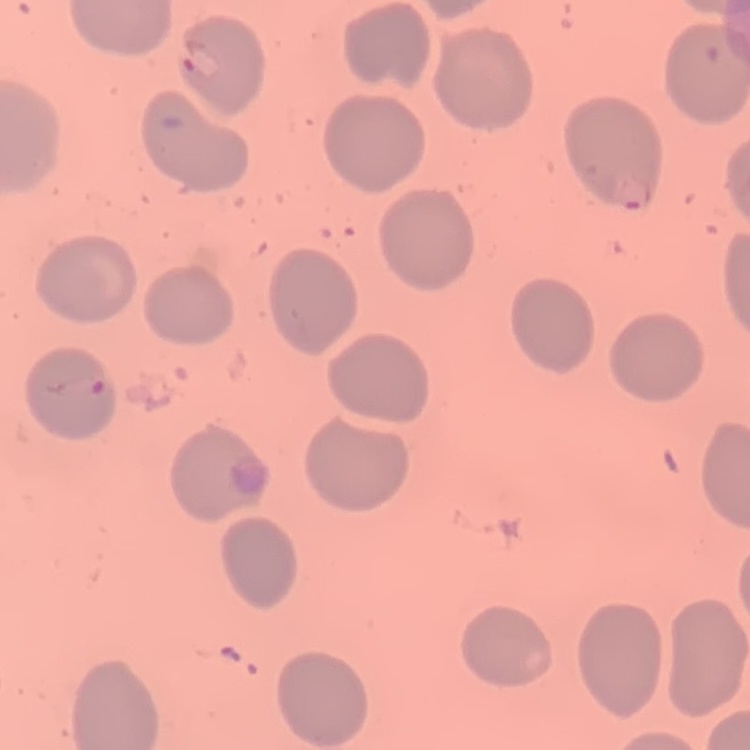

Summary:
  - Red blood cell morphology: no rouleaux formation
  - Preparation: thin blood film
  - Stain: Field's or Giemsa
  - Image type: square crop of a larger photomicrograph